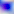

Captured at 400x magnification. Micrograph. Toxoplasma gondii is seen.